State the preparation type.
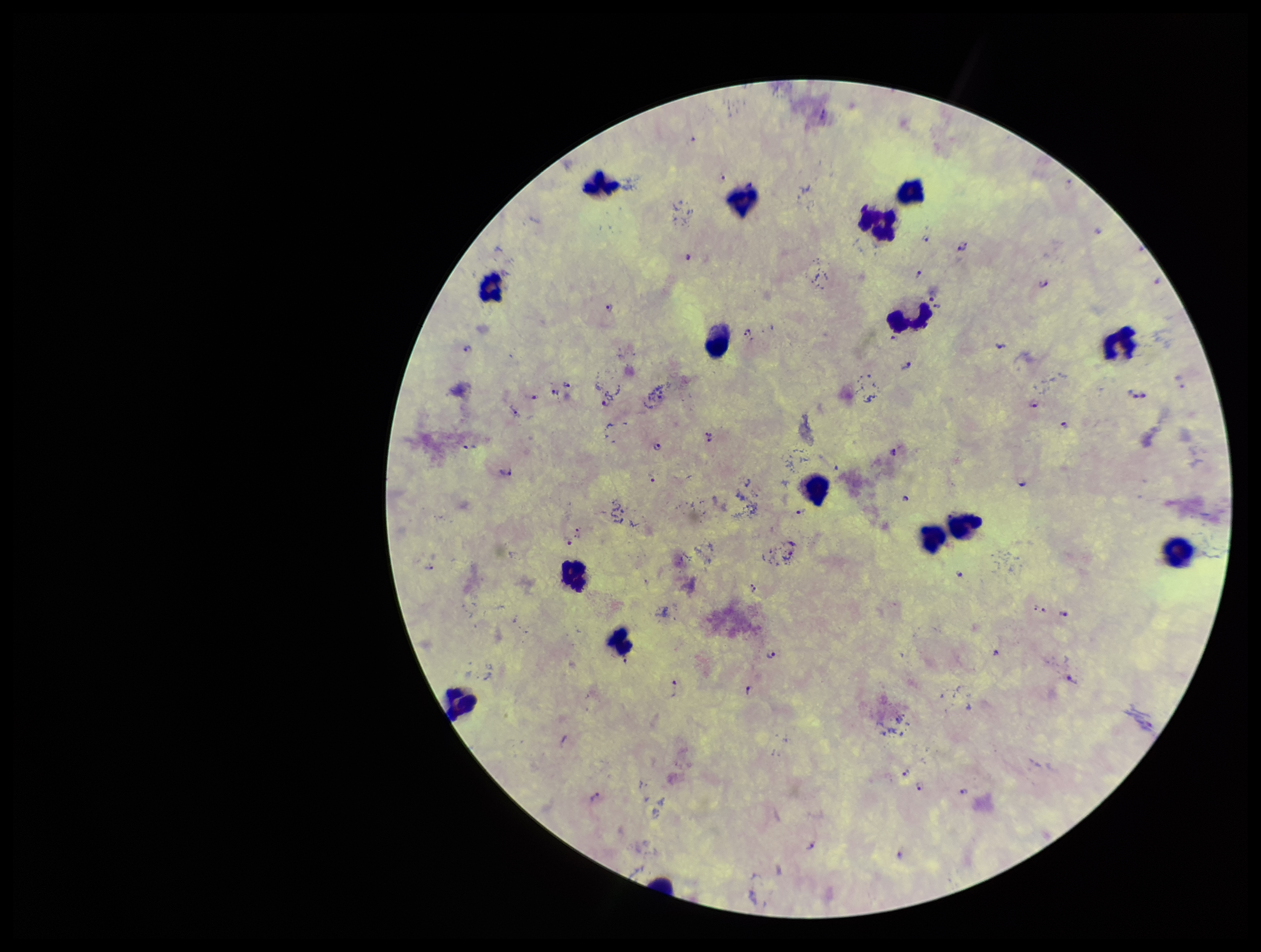
Thick.

Plasmodium parasites = identified
leukocyte count = 15
field of view = one from this slide
parasite count = 47
patient malaria status = infected
stain = Giemsa
capture = smartphone photograph through the microscope eyepiece
image size = 1261×952 pixels
species reported for this patient = Plasmodium falciparum